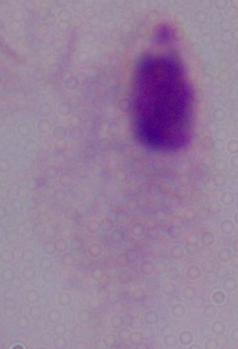

magnification = 1000x
identification = trichomonad
modality = micrograph